Assess the morphology of the red blood cells.
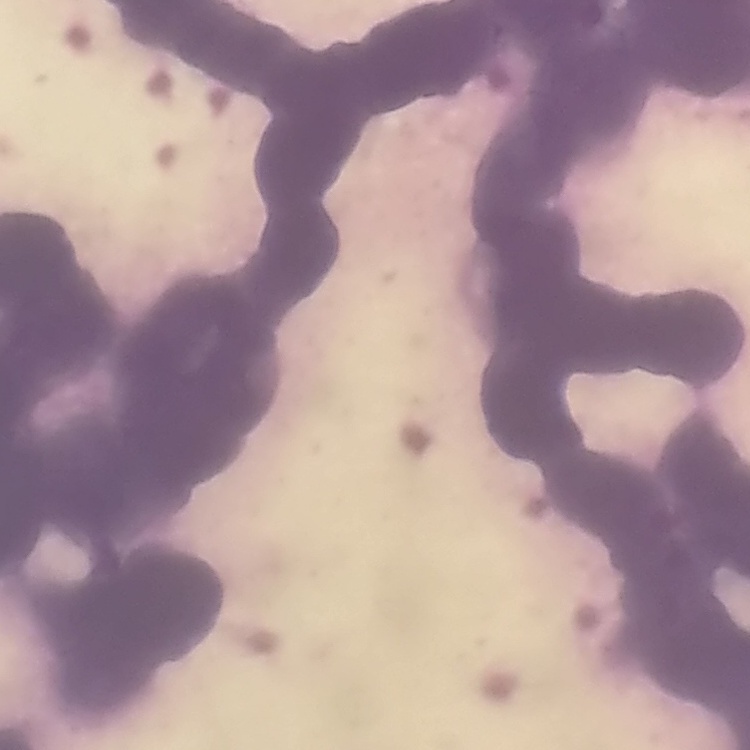

Rouleaux formation.

Stained with either Field's or Giemsa. Thin blood smear. One tile cut from a larger photomicrograph.